State the blood parasite species.
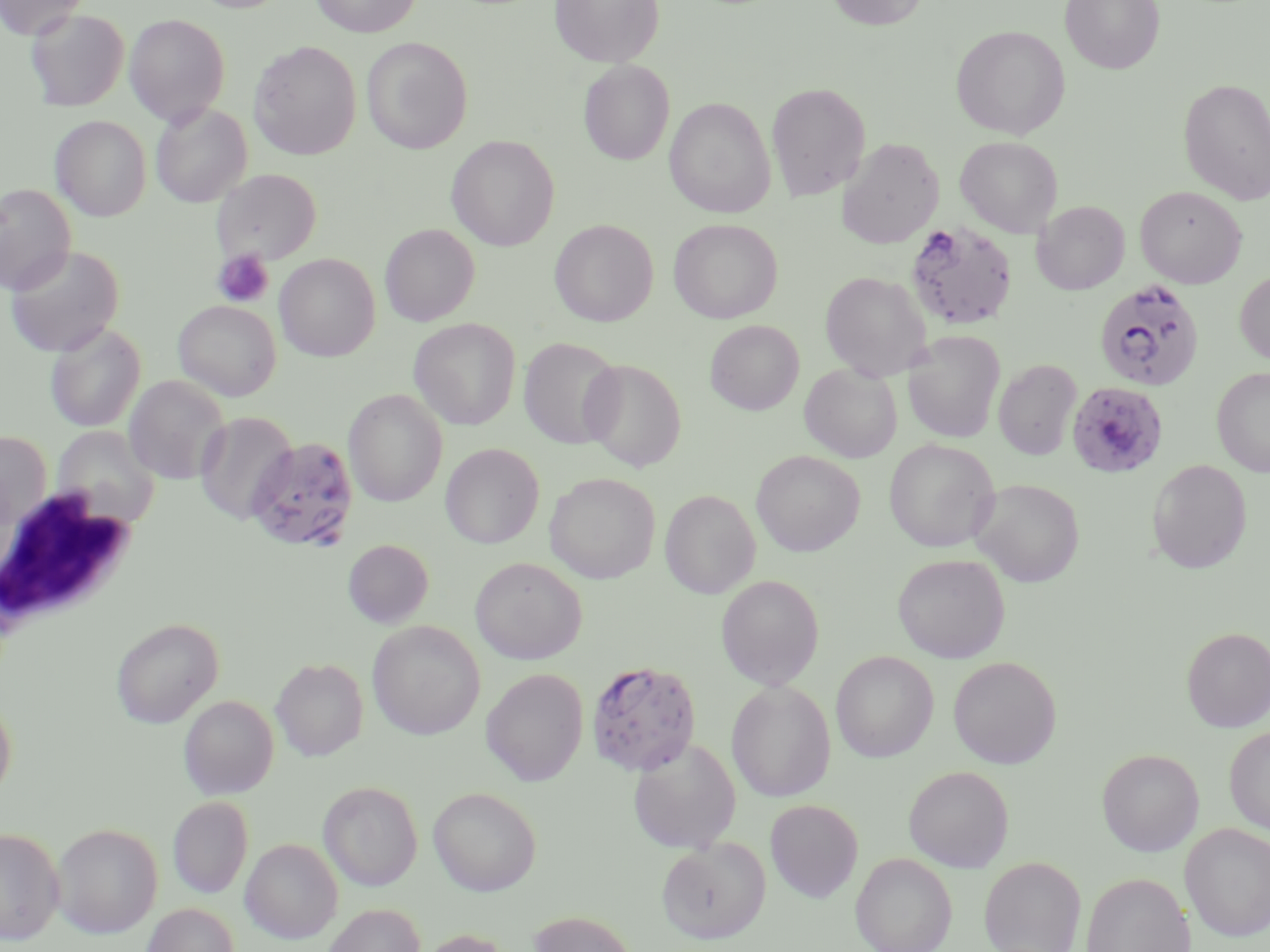

Plasmodium falciparum.

field of view = one of a larger specimen
modality = light microscopy
uninfected red blood cell locations = approximate bounding boxes as [x1, y1, x2, y2] in pixels: [0, 0, 88, 39], [190, 0, 291, 13], [311, 0, 420, 37], [550, 0, 664, 67], [826, 0, 929, 30], [1060, 0, 1165, 74], [25, 8, 129, 111], [124, 14, 230, 126], [951, 25, 1070, 139], [361, 37, 472, 154], [249, 41, 361, 160], [578, 60, 675, 165], [1178, 78, 1270, 205], [767, 82, 870, 201], [664, 97, 776, 217], [150, 102, 252, 207], [51, 116, 151, 222], [446, 135, 560, 251], [955, 136, 1062, 237], [839, 138, 943, 248], [212, 168, 322, 265], [0, 183, 76, 295], [1135, 186, 1247, 288], [1032, 200, 1130, 295], [549, 219, 658, 326], [668, 219, 783, 323], [380, 224, 479, 326], [4, 245, 125, 357], [275, 253, 380, 361], [819, 270, 931, 381], [1235, 270, 1270, 365], [173, 299, 281, 401], [409, 318, 521, 430], [705, 320, 804, 415], [45, 323, 146, 432], [903, 331, 1005, 443], [518, 337, 625, 449], [579, 358, 687, 472], [993, 358, 1082, 461], [800, 363, 902, 463], [1212, 367, 1270, 477], [123, 375, 230, 485], [343, 388, 448, 506], [195, 412, 296, 525], [51, 424, 161, 528], [0, 430, 51, 534], [883, 439, 999, 552], [440, 443, 544, 549], [751, 450, 865, 556], [1147, 459, 1252, 574], [544, 472, 661, 583], [970, 478, 1085, 587], [660, 489, 760, 598], [343, 539, 433, 628], [892, 552, 1010, 663], [470, 556, 587, 664], [716, 574, 824, 690], [110, 617, 224, 728], [367, 620, 485, 740], [1181, 627, 1270, 732], [831, 651, 938, 762], [948, 656, 1061, 769], [271, 657, 369, 761], [481, 667, 588, 786], [726, 680, 836, 803], [0, 691, 17, 804], [179, 695, 279, 799], [1224, 725, 1270, 833], [628, 738, 741, 854], [1097, 748, 1204, 856], [904, 765, 1014, 872], [318, 780, 423, 891], [428, 786, 542, 896], [168, 796, 253, 898], [765, 799, 863, 902], [52, 823, 163, 938], [1180, 823, 1270, 942], [0, 828, 64, 945], [240, 837, 344, 944], [657, 837, 771, 944], [851, 852, 957, 952], [979, 857, 1086, 952], [1081, 872, 1195, 952], [142, 903, 239, 952], [322, 903, 425, 952], [528, 911, 638, 952], [415, 928, 515, 952]
white blood cell locations = approximate bounding boxes as [x1, y1, x2, y2] in pixels: [0, 486, 141, 631]
magnification = 1000x
image size = 1270×952 pixels
platelet locations = approximate bounding boxes as [x1, y1, x2, y2] in pixels: [213, 249, 274, 307]
stain = May-Grünwald-Giemsa
preparation = thin blood smear
Plasmodium falciparum-infected red blood cell locations = approximate bounding boxes as [x1, y1, x2, y2] in pixels: [905, 220, 1018, 332], [1094, 278, 1205, 392], [1066, 380, 1168, 478], [240, 435, 360, 552], [586, 659, 701, 776]